Name the blood parasite species.
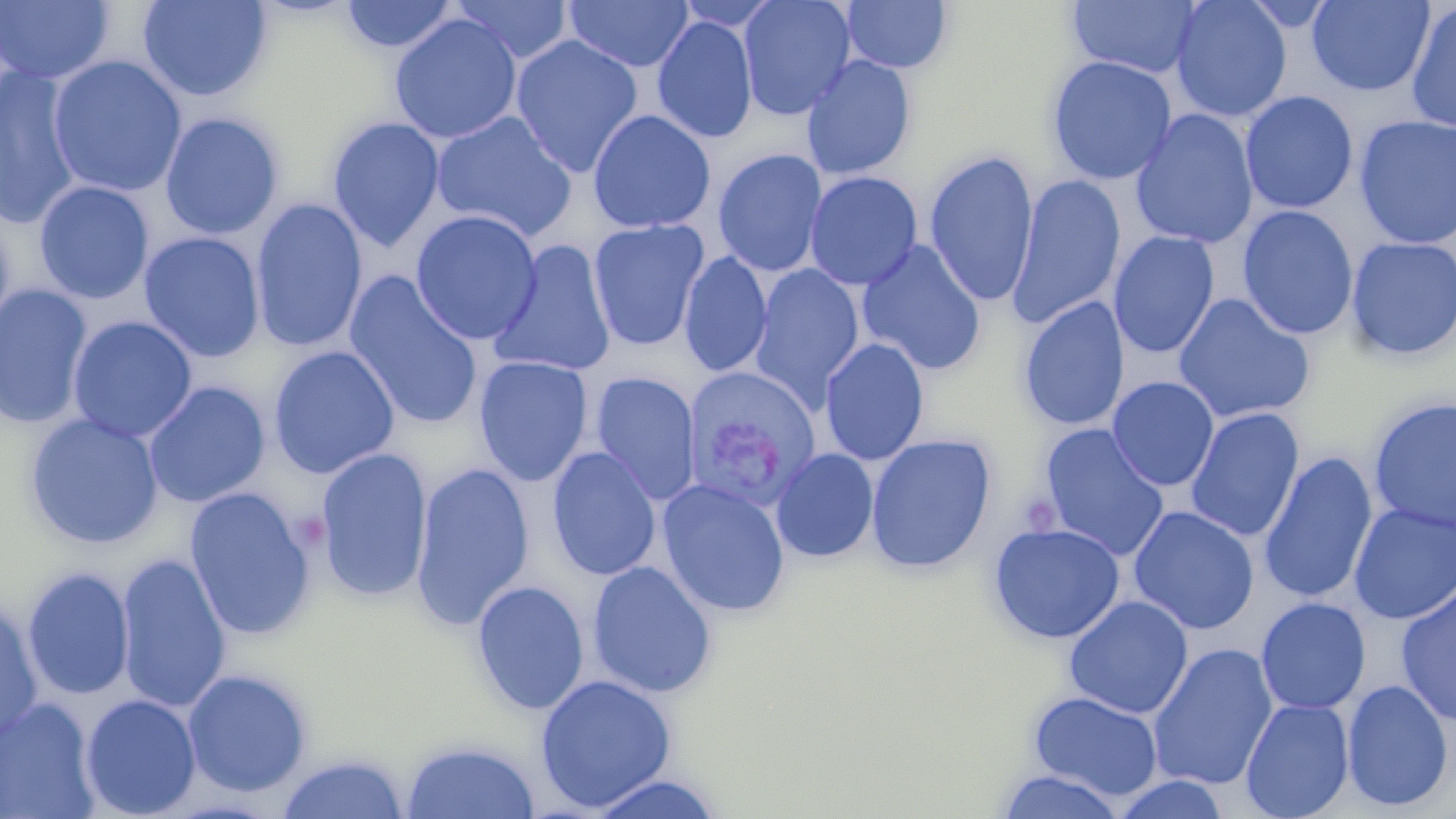
Plasmodium vivax.

Summary:
  - Coordinate format: approximate bounding boxes as named x1/y1/x2/y2 corners in pixels
  - Plasmodium vivax-infected red blood cell locations: (x1=682, y1=372, x2=828, y2=503)
  - Uninfected red blood cell locations: (x1=137, y1=0, x2=273, y2=102), (x1=339, y1=0, x2=461, y2=55), (x1=448, y1=0, x2=575, y2=64), (x1=564, y1=0, x2=693, y2=72), (x1=737, y1=0, x2=856, y2=120), (x1=840, y1=0, x2=954, y2=74), (x1=1066, y1=0, x2=1202, y2=79), (x1=1170, y1=0, x2=1292, y2=122), (x1=1306, y1=0, x2=1434, y2=96), (x1=0, y1=1, x2=114, y2=85), (x1=1405, y1=3, x2=1456, y2=133), (x1=388, y1=14, x2=522, y2=145), (x1=652, y1=15, x2=758, y2=143), (x1=511, y1=34, x2=644, y2=177), (x1=801, y1=54, x2=917, y2=180), (x1=46, y1=55, x2=188, y2=198), (x1=1046, y1=55, x2=1177, y2=186), (x1=0, y1=65, x2=85, y2=230), (x1=1240, y1=91, x2=1358, y2=214), (x1=1130, y1=108, x2=1260, y2=250), (x1=588, y1=109, x2=716, y2=233), (x1=431, y1=110, x2=578, y2=244), (x1=159, y1=112, x2=284, y2=240), (x1=1353, y1=114, x2=1456, y2=250), (x1=326, y1=116, x2=446, y2=252), (x1=712, y1=148, x2=828, y2=277), (x1=923, y1=149, x2=1039, y2=307), (x1=804, y1=170, x2=923, y2=291), (x1=1007, y1=173, x2=1126, y2=330), (x1=34, y1=180, x2=155, y2=305), (x1=250, y1=198, x2=368, y2=353), (x1=1236, y1=205, x2=1359, y2=340), (x1=0, y1=207, x2=16, y2=344), (x1=410, y1=209, x2=542, y2=345), (x1=587, y1=219, x2=709, y2=351), (x1=1108, y1=230, x2=1220, y2=359), (x1=138, y1=232, x2=266, y2=363), (x1=1346, y1=236, x2=1456, y2=362), (x1=857, y1=240, x2=987, y2=376), (x1=489, y1=241, x2=616, y2=378), (x1=678, y1=251, x2=773, y2=378), (x1=748, y1=265, x2=865, y2=411), (x1=344, y1=271, x2=485, y2=431), (x1=0, y1=284, x2=93, y2=430), (x1=1173, y1=293, x2=1315, y2=424), (x1=1018, y1=297, x2=1130, y2=432), (x1=67, y1=316, x2=198, y2=443), (x1=819, y1=338, x2=929, y2=466), (x1=268, y1=345, x2=400, y2=479), (x1=474, y1=355, x2=593, y2=487), (x1=590, y1=371, x2=701, y2=506), (x1=1107, y1=376, x2=1219, y2=491), (x1=143, y1=381, x2=270, y2=509), (x1=1367, y1=396, x2=1456, y2=535), (x1=1185, y1=408, x2=1304, y2=543), (x1=24, y1=413, x2=163, y2=549), (x1=1038, y1=424, x2=1169, y2=561), (x1=865, y1=434, x2=996, y2=573), (x1=314, y1=446, x2=433, y2=603), (x1=546, y1=447, x2=662, y2=582), (x1=770, y1=447, x2=879, y2=563), (x1=1258, y1=451, x2=1378, y2=605), (x1=411, y1=461, x2=535, y2=629), (x1=656, y1=478, x2=791, y2=618), (x1=184, y1=486, x2=317, y2=642), (x1=1349, y1=503, x2=1456, y2=624), (x1=1128, y1=506, x2=1260, y2=635), (x1=988, y1=522, x2=1126, y2=644), (x1=115, y1=551, x2=232, y2=714), (x1=587, y1=561, x2=718, y2=699), (x1=21, y1=566, x2=135, y2=701), (x1=471, y1=580, x2=589, y2=715), (x1=1395, y1=582, x2=1456, y2=727), (x1=1064, y1=595, x2=1193, y2=719), (x1=1256, y1=597, x2=1371, y2=715), (x1=0, y1=600, x2=44, y2=744), (x1=1147, y1=643, x2=1279, y2=790), (x1=182, y1=669, x2=313, y2=798), (x1=534, y1=674, x2=677, y2=812), (x1=1341, y1=678, x2=1454, y2=812), (x1=1029, y1=691, x2=1163, y2=800), (x1=79, y1=694, x2=201, y2=819), (x1=1, y1=697, x2=102, y2=819), (x1=1240, y1=698, x2=1355, y2=819), (x1=400, y1=739, x2=541, y2=818), (x1=275, y1=752, x2=410, y2=819), (x1=995, y1=769, x2=1127, y2=819), (x1=586, y1=773, x2=724, y2=818), (x1=1111, y1=773, x2=1230, y2=818)
  - Preparation: thin blood film
  - Magnification: 1000x
  - Modality: light microscopy
  - Stain: May-Grünwald-Giemsa
  - Image size: 1456×819 pixels
  - Field of view: one of a larger specimen